Outline each blood parasite and name the species.
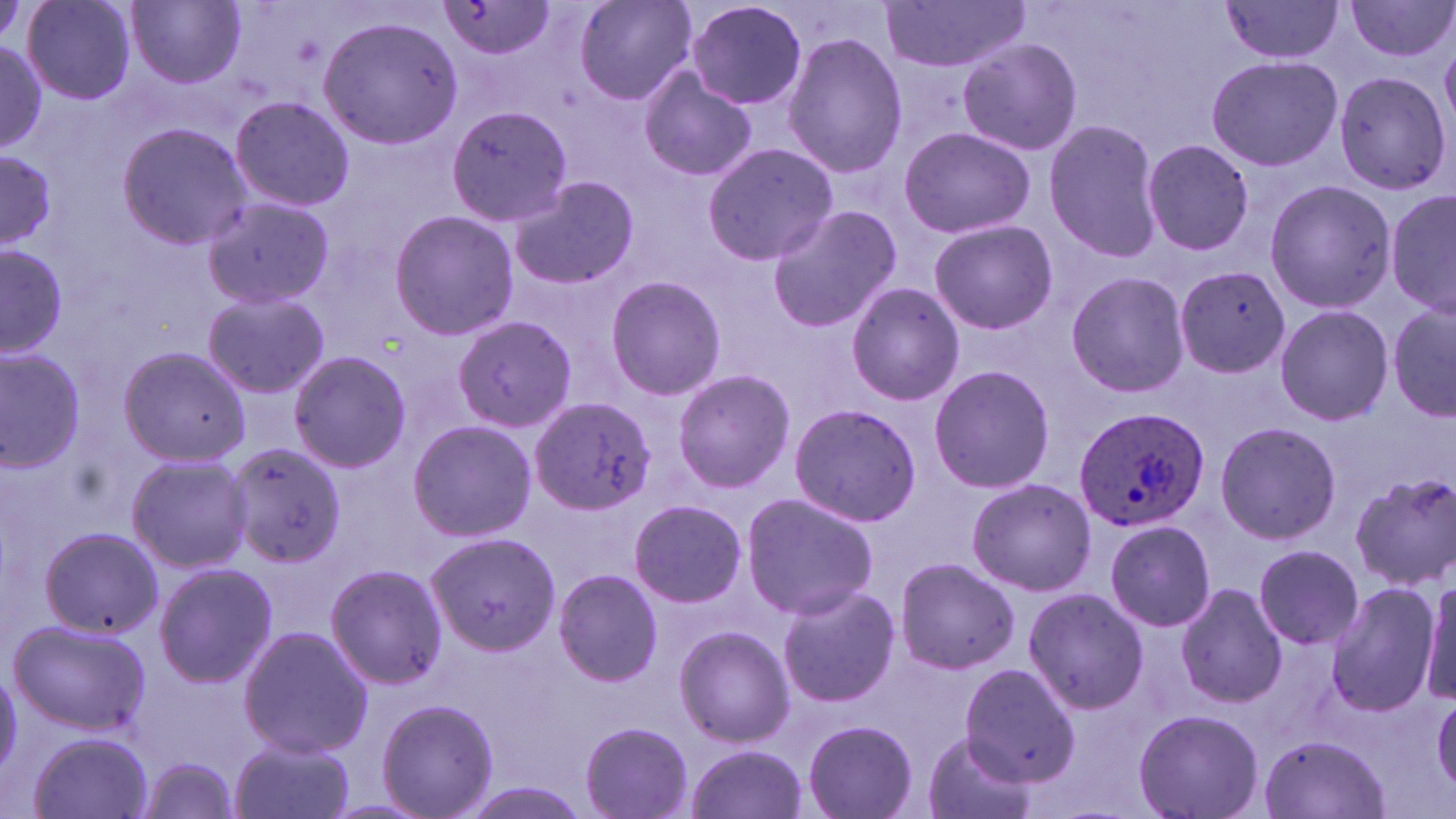

Approximate bounding boxes as (x1, y1, x2, y2) in pixels.
Plasmodium ovale-infected red blood cells: (1071, 406, 1209, 533).
No Plasmodium falciparum, Plasmodium malariae, Plasmodium vivax, Babesia divergens, or Trypanosoma brucei observed.

slide_level_diagnosis: Plasmodium ovale
preparation: thin blood film
uninfected_red_blood_cell_locations: 'approximate bounding boxes as (x1, y1, x2, y2) in pixels: (21, 0, 138, 106), (129, 0, 246, 88), (435, 0, 558, 62), (575, 0, 698, 106), (684, 0, 809, 110), (1345, 0, 1455, 63), (880, 1, 1031, 73), (1219, 1, 1347, 63), (317, 15, 465, 152), (781, 32, 908, 181), (0, 35, 48, 155), (957, 36, 1083, 157), (1206, 56, 1343, 171), (636, 68, 758, 185), (1337, 74, 1452, 194), (226, 97, 356, 212), (446, 104, 575, 226), (1043, 117, 1163, 264), (116, 122, 253, 249), (899, 125, 1035, 240), (1141, 138, 1255, 256), (701, 141, 839, 266), (0, 149, 59, 249), (506, 174, 642, 293), (1268, 177, 1394, 314), (1385, 188, 1455, 321), (200, 197, 334, 310), (765, 202, 902, 335), (389, 209, 518, 341), (927, 219, 1058, 335), (1, 244, 67, 362), (1175, 269, 1294, 380), (1065, 271, 1192, 397), (605, 274, 727, 400), (844, 281, 965, 406), (201, 290, 331, 400), (1387, 301, 1456, 423), (1273, 303, 1393, 425), (452, 314, 578, 433), (117, 346, 253, 465), (0, 351, 84, 469), (289, 351, 409, 471), (927, 365, 1056, 495), (672, 368, 795, 494), (530, 396, 658, 515), (789, 403, 920, 528), (407, 419, 537, 540), (1212, 421, 1343, 544), (224, 442, 347, 571), (126, 455, 253, 572), (1350, 472, 1456, 590), (965, 477, 1096, 596), (978, 491, 1117, 678), (740, 493, 879, 619), (627, 498, 748, 609), (1103, 517, 1215, 633), (37, 526, 162, 639), (428, 532, 558, 655), (1253, 544, 1364, 649), (895, 556, 1020, 675), (152, 562, 278, 687), (324, 563, 448, 690), (552, 570, 662, 687), (1418, 573, 1456, 708), (776, 582, 901, 710), (1175, 582, 1286, 708), (1325, 583, 1441, 717), (1022, 587, 1148, 715), (9, 620, 152, 735), (238, 625, 374, 758), (674, 626, 794, 749), (958, 664, 1082, 786), (0, 665, 22, 775), (1431, 694, 1456, 798), (377, 698, 499, 819), (1132, 707, 1264, 819), (802, 719, 918, 818), (578, 722, 695, 818), (26, 729, 155, 819), (920, 731, 1038, 819), (1258, 733, 1390, 819), (227, 735, 358, 819), (682, 743, 810, 819), (138, 759, 242, 816)'
image_size: 1456×819 pixels
stain: May-Grünwald-Giemsa
modality: optical microscopy
field_of_view: single
magnification: 1000x